Assess the morphology of the erythrocytes.
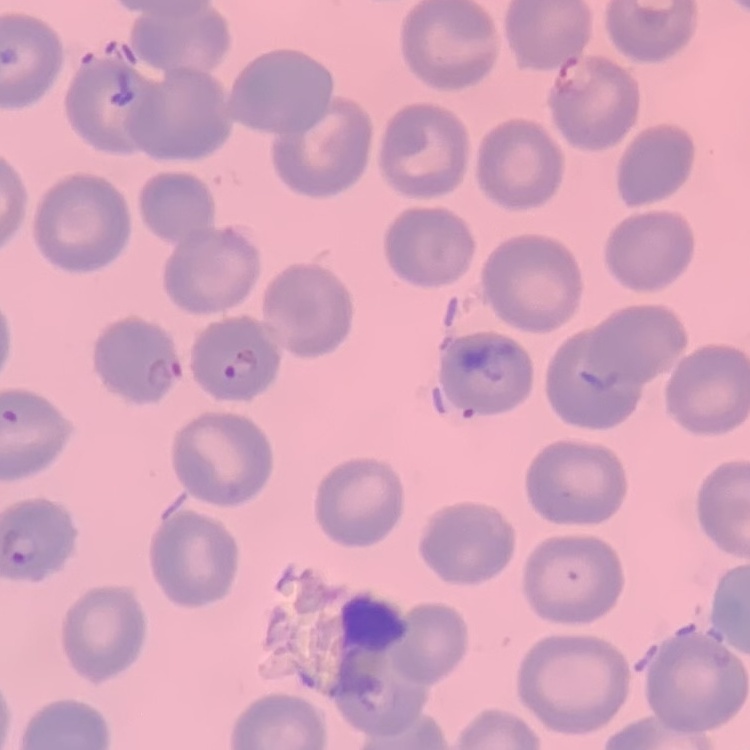
No rouleaux formation.

Thin blood film. One tile cut from a larger photomicrograph. Stained with either Field's or Giemsa.